Assess this cell for malaria.
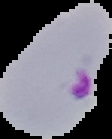

Parasitized.

{
  "preparation": "thin blood smear",
  "image_type": "segmented cell region on a black background",
  "image_size": "112×139 pixels"
}